Classify this cell by malaria status.
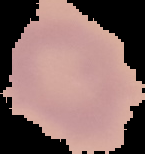
Uninfected.

Segmented cell region on a black background. Image is 145×154 pixels. From a thin blood film.